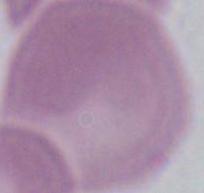

{
  "modality": "photomicrograph",
  "magnification": "1000x",
  "identification": "erythrocyte"
}